Classify this cell by malaria status.
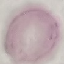

It is uninfected.

Thin blood film. Giemsa-stained preparation. Photographed with a smartphone camera at the microscope eyepiece. Cell patch, automatically extracted from a larger field of view and resized to 64 × 64 pixels.